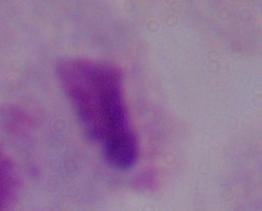
A trichomonad is shown. Micrograph. Captured at 1000x magnification.